Classify this cell by malaria status.
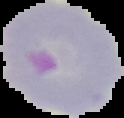

It is parasitized.

image_type: segmented cell region with the area outside set to black
preparation: thin blood smear
image_size: 124×118 pixels